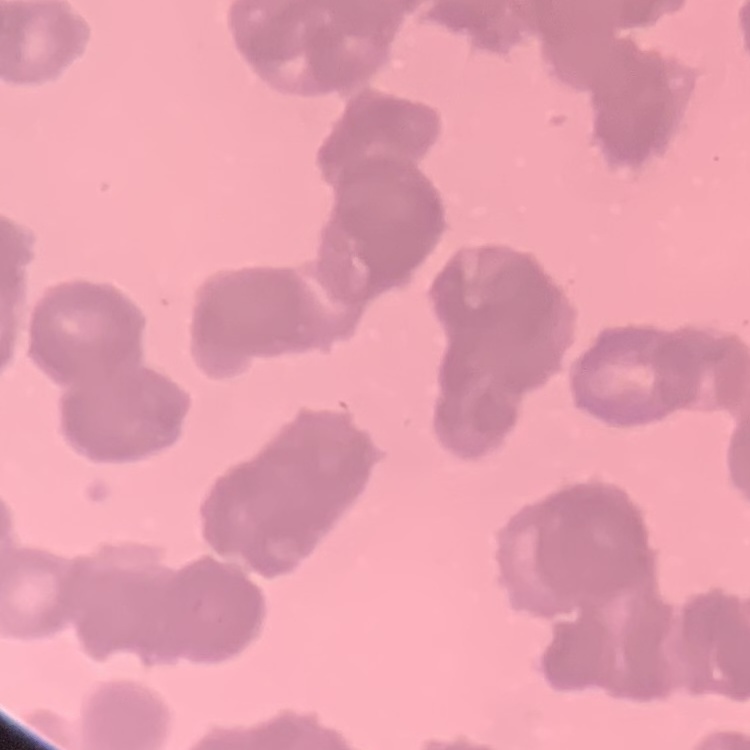

The red blood cells exhibit rouleaux formation. Field's or Giemsa stain. One tile cut from a larger photomicrograph. Thin peripheral smear.